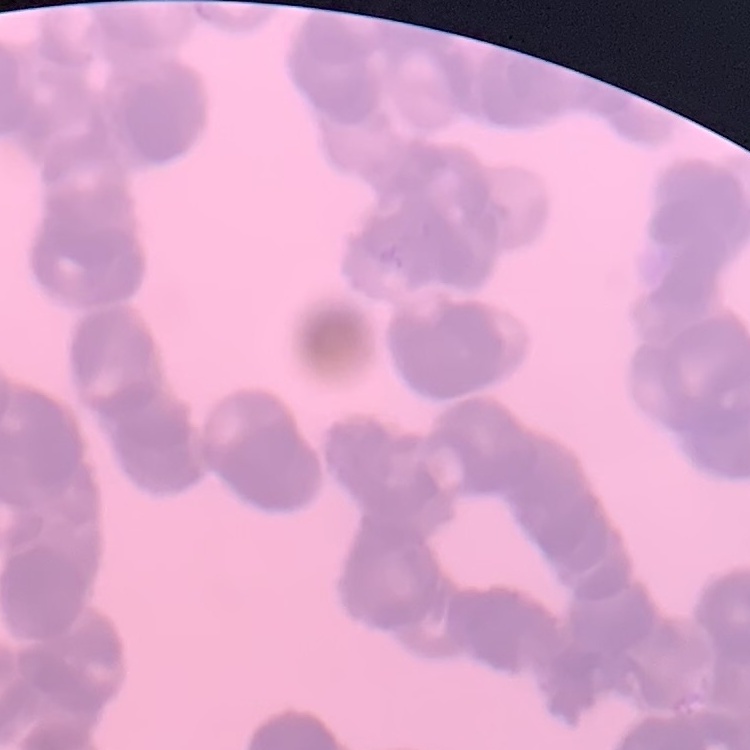
red_blood_cell_morphology: rouleaux formation
stain: Field's or Giemsa
preparation: thin blood film
image_type: square crop of a larger photomicrograph